Classify this cell by malaria status.
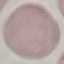

It is uninfected.

Summary:
  - Capture: smartphone camera at the microscope eyepiece
  - Preparation: thin blood film
  - Stain: Giemsa
  - Image type: cell patch, automatically extracted from a larger field of view and resized to 64 × 64 pixels